Locate every blood parasite and identify its species.
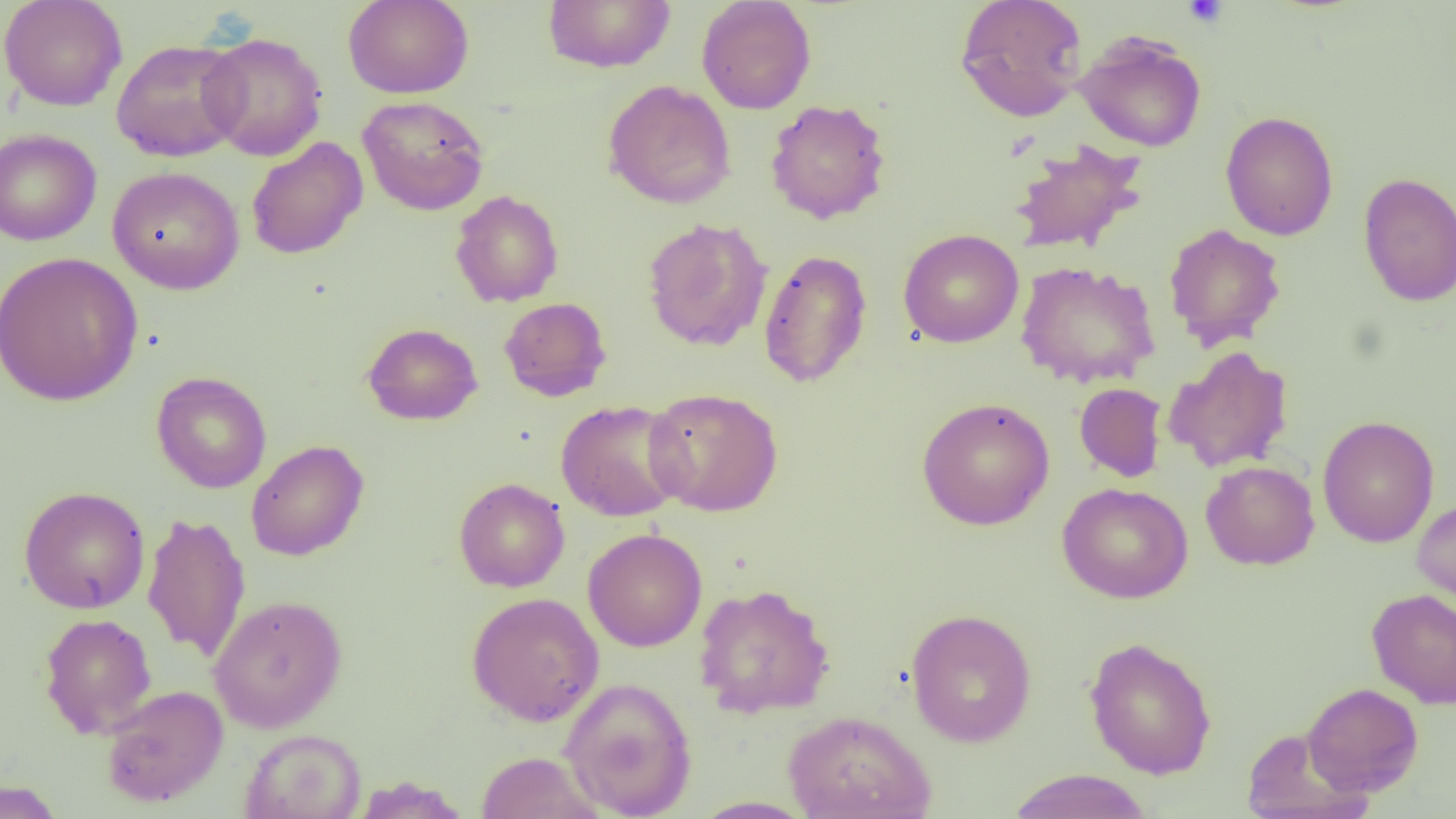

No blood parasites seen.

{
  "slide_level_diagnosis": "no evidence of blood parasites",
  "image_size": "1456×819 pixels",
  "platelet_locations": "approximate bounding boxes as (x1,y1)-(x2,y2) corner pairs in pixels: (1182,0)-(1228,27)",
  "modality": "optical microscopy",
  "magnification": "1000x",
  "uninfected_red_blood_cell_locations": "approximate bounding boxes as (x1,y1)-(x2,y2) corner pairs in pixels: (0,0)-(128,111), (343,0)-(474,99), (696,0)-(816,114), (954,0)-(1089,122), (542,1)-(676,72), (1074,31)-(1207,152), (199,32)-(328,161), (111,38)-(248,162), (603,80)-(737,209), (357,95)-(489,215), (765,99)-(891,224), (1220,111)-(1338,241), (0,129)-(102,246), (246,137)-(368,260), (1008,139)-(1148,256), (107,166)-(245,295), (1358,172)-(1456,306), (450,190)-(564,307), (642,217)-(773,352), (1164,223)-(1286,351), (898,229)-(1024,348), (758,249)-(872,388), (0,251)-(144,406), (1016,261)-(1160,389), (499,297)-(612,401), (362,322)-(483,426), (1164,345)-(1293,474), (151,371)-(272,493), (1074,383)-(1167,483), (644,387)-(783,516), (916,396)-(1055,530), (555,400)-(688,521), (1317,415)-(1439,548), (246,439)-(369,561), (1201,460)-(1320,570), (454,477)-(570,593), (1057,482)-(1193,604), (19,486)-(150,614), (1412,497)-(1456,615), (142,511)-(250,663), (582,528)-(707,652), (693,583)-(835,719), (1367,588)-(1456,709), (466,592)-(604,725), (209,594)-(347,733), (906,608)-(1037,747), (40,613)-(157,739), (1084,636)-(1217,779), (559,677)-(698,818), (1302,682)-(1424,797), (101,685)-(228,808), (783,710)-(936,819), (1241,728)-(1370,818), (240,729)-(365,818), (476,751)-(603,819), (1005,769)-(1153,819), (353,776)-(471,818), (0,779)-(65,819), (692,796)-(814,818)",
  "preparation": "thin blood smear",
  "field_of_view": "one of a larger specimen"
}